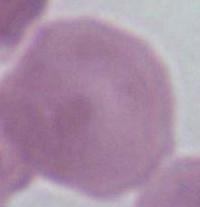
Summary:
  - Modality: micrograph
  - Identification: erythrocyte
  - Magnification: 1000x